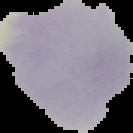

Summary:
  - Malaria status: uninfected
  - Preparation: thin blood film
  - Image type: cell region segmented out of the field of view; surrounding area masked to black
  - Image size: 133×133 pixels